Outline platelets.
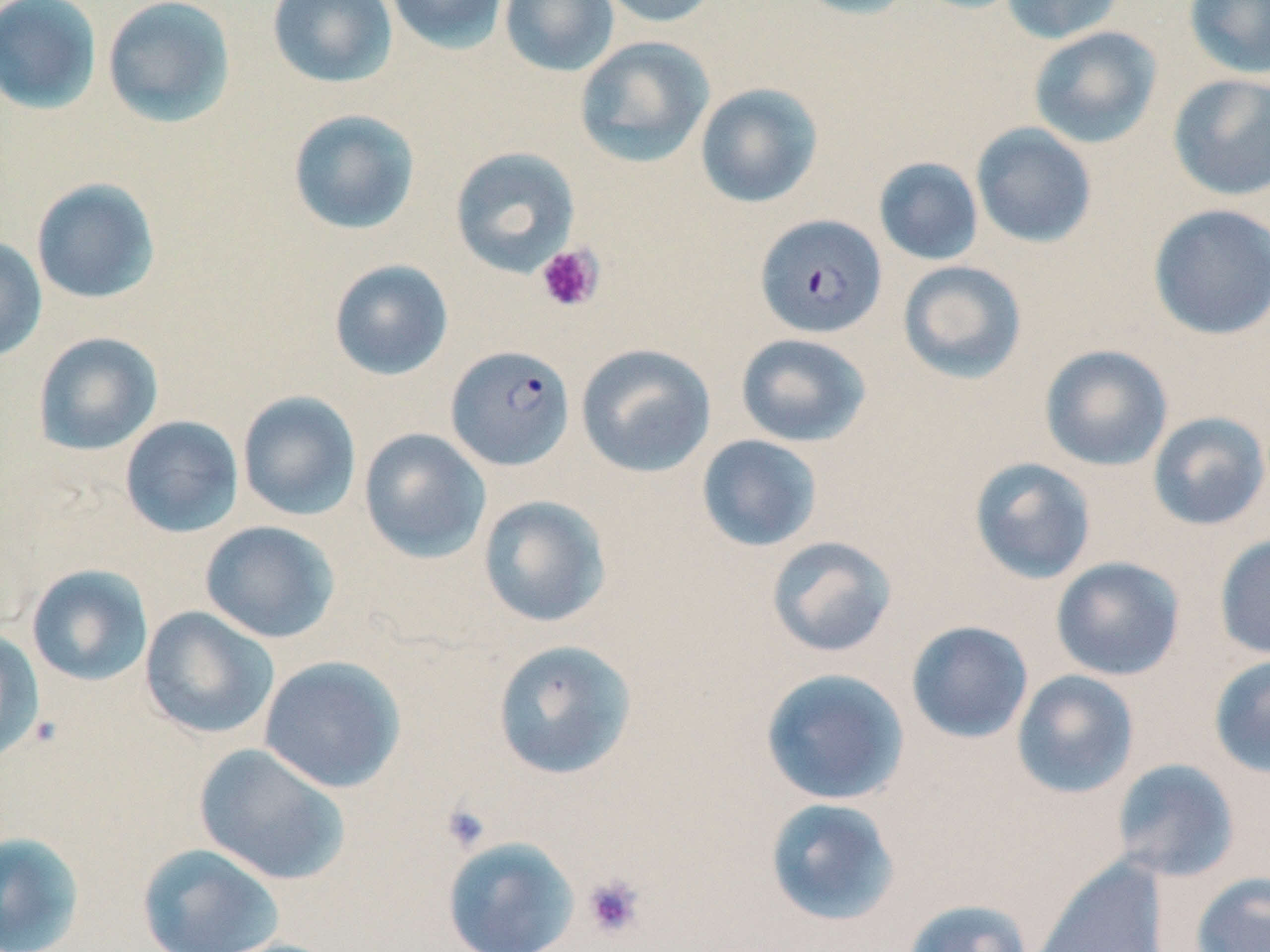

Approximate bounding boxes as [x1, y1, x2, y2] in pixels.
Platelets: [536, 244, 604, 313], [440, 802, 493, 853], [581, 874, 646, 940].

{
  "slide_level_diagnosis": "Plasmodium falciparum",
  "modality": "optical microscopy",
  "uninfected_red_blood_cell_locations": "approximate bounding boxes as [x1, y1, x2, y2] in pixels: [0, 0, 102, 115], [102, 0, 236, 128], [266, 0, 398, 88], [384, 0, 511, 54], [499, 0, 619, 76], [594, 0, 723, 27], [789, 0, 919, 20], [1000, 0, 1126, 45], [1183, 0, 1270, 79], [1028, 26, 1162, 149], [574, 36, 714, 168], [1167, 73, 1270, 201], [695, 83, 824, 208], [287, 109, 421, 235], [970, 122, 1098, 249], [449, 146, 581, 278], [873, 156, 984, 266], [31, 178, 161, 304], [1147, 203, 1270, 341], [0, 236, 47, 363], [328, 259, 454, 381], [897, 260, 1027, 385], [32, 331, 164, 456], [735, 333, 872, 448], [575, 343, 716, 478], [1039, 344, 1173, 471], [236, 390, 362, 522], [1147, 411, 1270, 532], [119, 415, 244, 538], [359, 428, 491, 564], [696, 434, 824, 553], [969, 456, 1097, 585], [477, 494, 612, 629], [200, 520, 340, 644], [1214, 533, 1270, 660], [765, 535, 898, 659], [1050, 556, 1186, 681], [26, 564, 154, 686], [139, 606, 280, 740], [905, 621, 1034, 744], [0, 628, 44, 762], [491, 639, 638, 780], [1208, 653, 1270, 779], [258, 655, 407, 794], [759, 667, 910, 806], [1010, 669, 1140, 799], [194, 743, 350, 886], [1111, 758, 1240, 882], [764, 797, 901, 927], [0, 831, 86, 952], [442, 836, 580, 952], [136, 842, 285, 952], [1029, 858, 1169, 952], [1190, 871, 1270, 952], [900, 898, 1034, 952], [206, 937, 347, 952]",
  "image_size": "1270×952 pixels",
  "plasmodium_falciparum_infected_red_blood_cell_locations": "approximate bounding boxes as [x1, y1, x2, y2] in pixels: [754, 213, 888, 339], [445, 344, 575, 471]",
  "field_of_view": "one of a larger specimen",
  "magnification": "1000x",
  "preparation": "thin blood smear",
  "stain": "May-Grünwald-Giemsa"
}